Comment on the morphology of the erythrocytes.
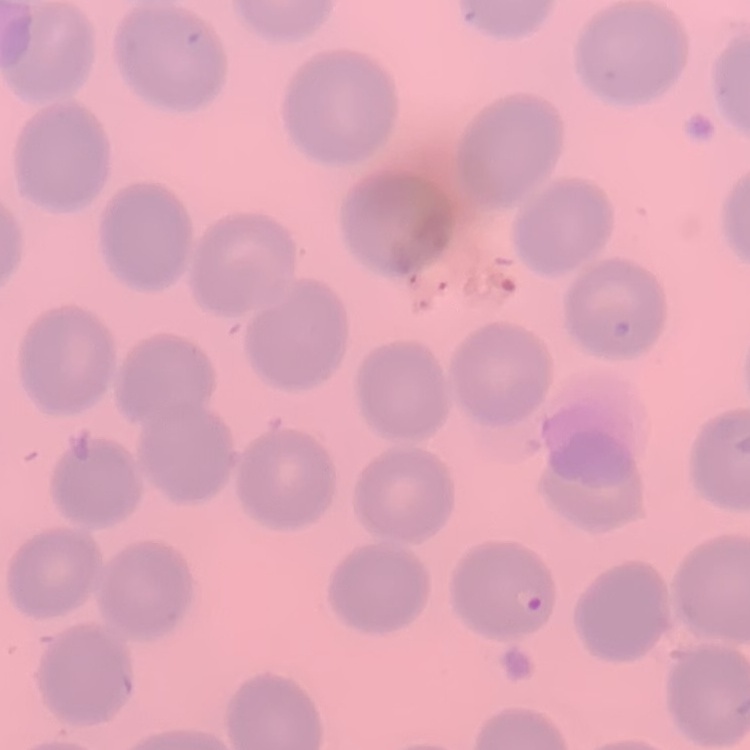

No rouleaux formation.

preparation = thin blood film
stain = Field's or Giemsa
image type = one tile cut from a larger photomicrograph